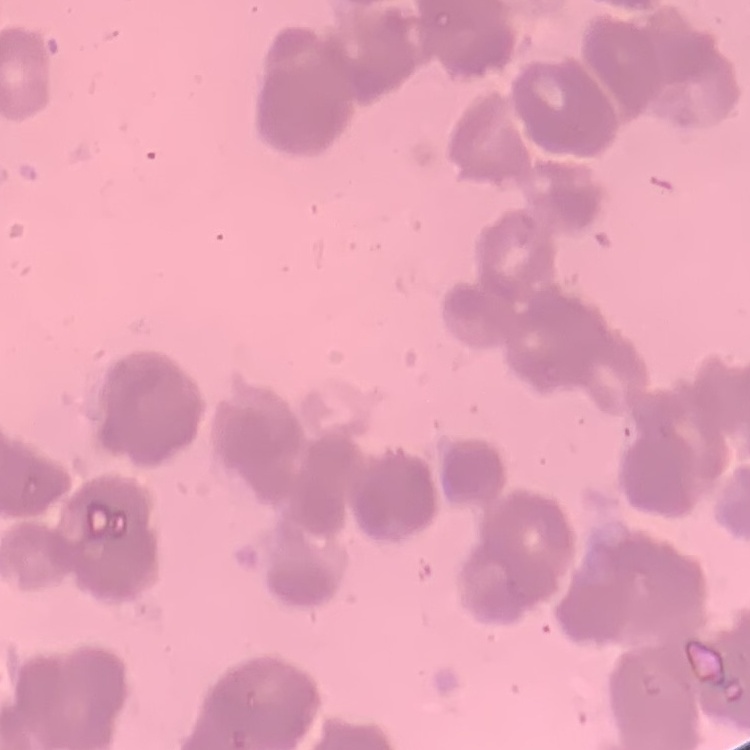
red_blood_cell_morphology: rouleaux formation
stain: Field's or Giemsa
image_type: one tile cut from a larger photomicrograph
preparation: thin peripheral smear